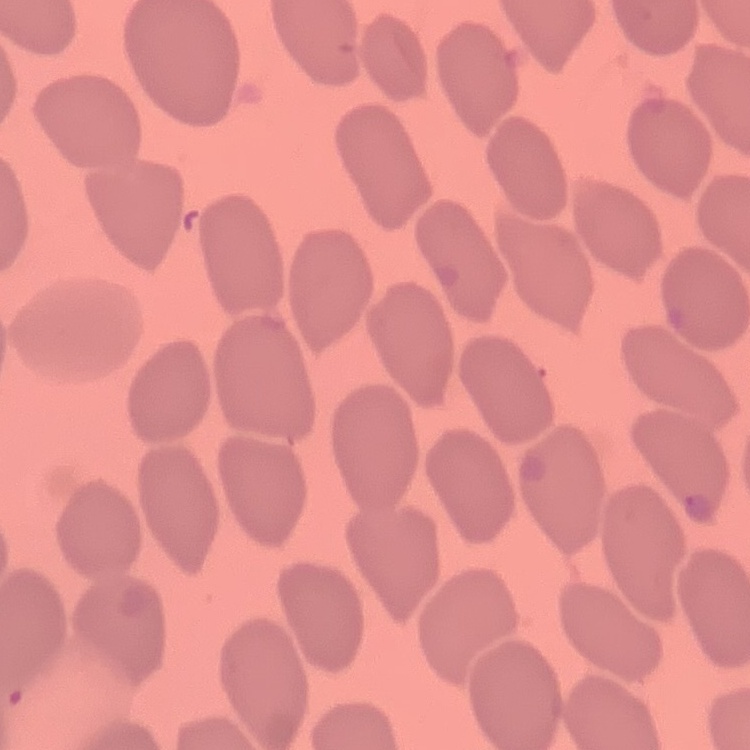
The red blood cells show no rouleaux formation. Thin peripheral smear. Square crop of a larger photomicrograph. Field's or Giemsa stain.